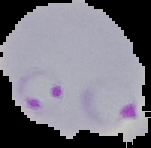
Summary:
  - Image size: 151×148 pixels
  - Malaria status: parasitized
  - Preparation: thin blood smear
  - Image type: segmented cell region on a black background